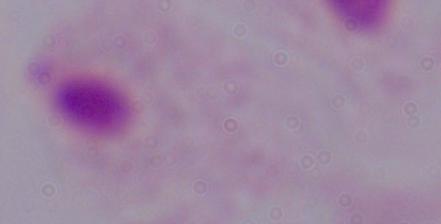 A trichomonad is seen. Captured at 1000x magnification. Micrograph.